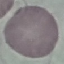
Summary:
  - Result: negative for malaria parasites
  - Capture: smartphone camera at the microscope eyepiece
  - Preparation: thin blood film
  - Stain: Giemsa
  - Image type: automatically extracted cell patch, resized to 64 × 64 pixels